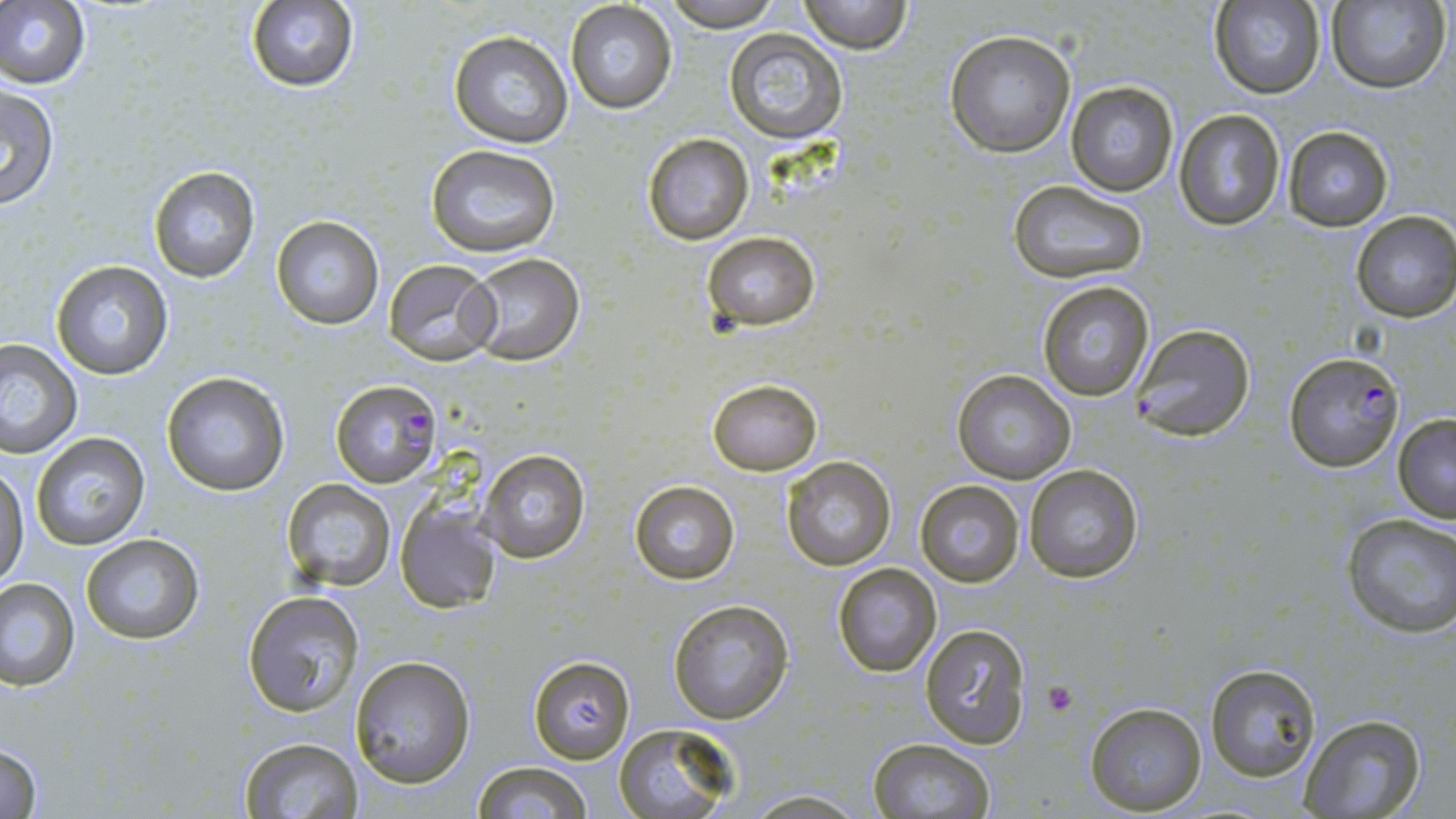

Approximate bounding boxes as [x1, y1, x2, y2] in pixels. Platelet locations: [1044, 682, 1077, 715]. Uninfected red blood cell locations: [661, 0, 782, 28], [797, 0, 912, 53], [244, 1, 358, 92], [1325, 1, 1449, 92], [0, 2, 91, 88], [565, 2, 677, 114], [1209, 2, 1326, 100], [724, 28, 848, 143], [945, 29, 1077, 157], [448, 30, 573, 148], [1065, 80, 1180, 197], [0, 84, 61, 210], [1173, 109, 1286, 229], [1282, 125, 1396, 231], [642, 133, 754, 244], [426, 146, 561, 258], [148, 167, 260, 282], [1008, 179, 1149, 284], [1351, 210, 1456, 322], [271, 215, 384, 330], [702, 231, 819, 331], [462, 253, 586, 366], [383, 258, 501, 364], [51, 259, 174, 380], [1036, 280, 1155, 402], [1128, 323, 1257, 443], [0, 338, 81, 457], [951, 368, 1077, 483], [160, 371, 290, 497], [707, 379, 822, 476], [1392, 414, 1456, 522], [29, 432, 152, 550], [477, 449, 591, 564], [782, 457, 895, 571], [1, 464, 28, 593], [1024, 464, 1145, 584], [278, 477, 396, 590], [914, 479, 1026, 587], [628, 480, 741, 585], [394, 499, 503, 613], [1341, 511, 1456, 638], [79, 532, 205, 644], [831, 563, 942, 677], [1, 578, 79, 689], [242, 591, 364, 717], [667, 599, 794, 723], [918, 623, 1034, 749], [527, 654, 636, 763], [349, 655, 476, 788], [1205, 664, 1323, 781], [1084, 703, 1206, 815], [1299, 715, 1425, 817], [611, 726, 738, 818], [867, 737, 995, 818], [237, 738, 365, 819], [0, 742, 45, 818], [470, 761, 594, 819], [739, 790, 868, 819]. Plasmodium falciparum-infected red blood cell locations: [1283, 351, 1406, 472], [330, 380, 443, 489]. Slide-level diagnosis: Plasmodium falciparum. May-Grünwald-Giemsa-stained preparation. Captured at 1000x magnification. Light microscopy. Single field of view. Thin blood film. Image is 1456×819 pixels.